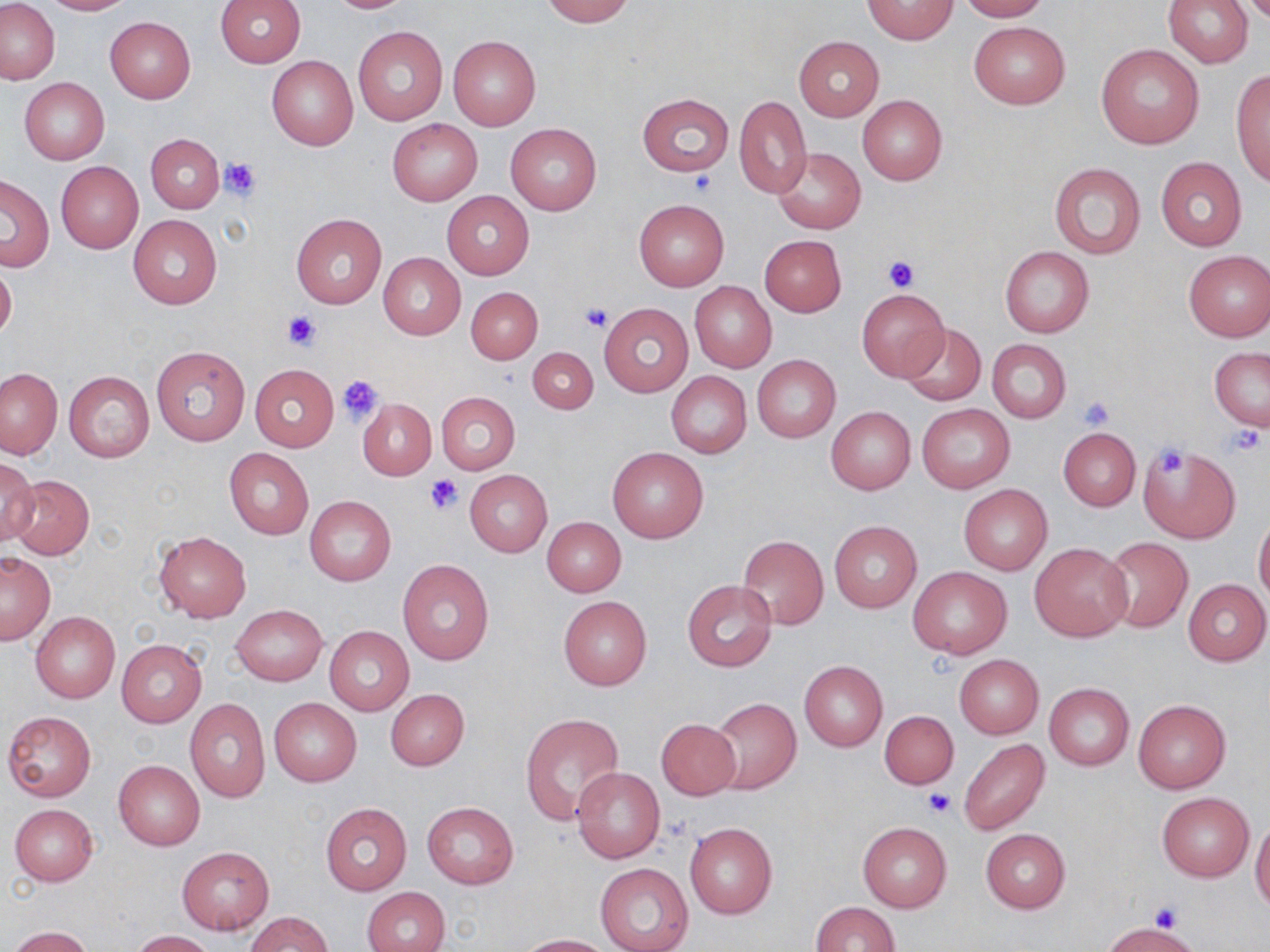

Summary:
  - Coordinate format: approximate bounding boxes as named x1/y1/x2/y2 corners in pixels
  - Platelet locations: (x1=221, y1=158, x2=261, y2=201), (x1=689, y1=172, x2=717, y2=195), (x1=880, y1=254, x2=921, y2=292), (x1=581, y1=302, x2=611, y2=332), (x1=281, y1=309, x2=323, y2=350), (x1=338, y1=372, x2=385, y2=423), (x1=1078, y1=396, x2=1117, y2=431), (x1=1223, y1=426, x2=1265, y2=461), (x1=1149, y1=443, x2=1190, y2=482), (x1=424, y1=473, x2=463, y2=515), (x1=922, y1=789, x2=954, y2=819), (x1=1150, y1=902, x2=1181, y2=934)
  - Uninfected red blood cell locations: (x1=1, y1=0, x2=60, y2=85), (x1=37, y1=0, x2=137, y2=15), (x1=324, y1=0, x2=418, y2=13), (x1=541, y1=0, x2=633, y2=26), (x1=863, y1=0, x2=957, y2=44), (x1=958, y1=0, x2=1048, y2=21), (x1=214, y1=1, x2=307, y2=66), (x1=1164, y1=1, x2=1253, y2=68), (x1=104, y1=16, x2=196, y2=103), (x1=968, y1=21, x2=1070, y2=110), (x1=353, y1=25, x2=447, y2=126), (x1=448, y1=35, x2=541, y2=131), (x1=794, y1=36, x2=885, y2=120), (x1=1096, y1=44, x2=1205, y2=150), (x1=267, y1=54, x2=359, y2=151), (x1=1231, y1=67, x2=1270, y2=187), (x1=20, y1=78, x2=109, y2=165), (x1=638, y1=93, x2=733, y2=177), (x1=857, y1=94, x2=948, y2=185), (x1=734, y1=96, x2=812, y2=197), (x1=386, y1=118, x2=482, y2=207), (x1=506, y1=123, x2=601, y2=216), (x1=146, y1=133, x2=225, y2=214), (x1=773, y1=147, x2=866, y2=234), (x1=1156, y1=157, x2=1247, y2=250), (x1=56, y1=162, x2=142, y2=254), (x1=1048, y1=163, x2=1146, y2=259), (x1=0, y1=175, x2=54, y2=271), (x1=442, y1=190, x2=534, y2=280), (x1=634, y1=200, x2=728, y2=291), (x1=290, y1=212, x2=387, y2=309), (x1=128, y1=214, x2=223, y2=310), (x1=759, y1=234, x2=846, y2=317), (x1=1000, y1=245, x2=1094, y2=337), (x1=1184, y1=250, x2=1270, y2=343), (x1=378, y1=252, x2=466, y2=339), (x1=0, y1=258, x2=17, y2=344), (x1=690, y1=281, x2=777, y2=372), (x1=467, y1=287, x2=543, y2=363), (x1=857, y1=288, x2=950, y2=380), (x1=599, y1=304, x2=693, y2=397), (x1=897, y1=322, x2=985, y2=406), (x1=987, y1=340, x2=1071, y2=422), (x1=150, y1=344, x2=250, y2=446), (x1=527, y1=347, x2=598, y2=414), (x1=1210, y1=347, x2=1269, y2=430), (x1=751, y1=355, x2=841, y2=443), (x1=249, y1=363, x2=339, y2=451), (x1=1, y1=368, x2=62, y2=459), (x1=64, y1=371, x2=154, y2=462), (x1=666, y1=372, x2=751, y2=457), (x1=435, y1=392, x2=520, y2=475), (x1=358, y1=399, x2=437, y2=480), (x1=917, y1=403, x2=1015, y2=493), (x1=825, y1=406, x2=915, y2=494), (x1=1058, y1=428, x2=1141, y2=511), (x1=1139, y1=444, x2=1242, y2=544), (x1=608, y1=446, x2=709, y2=543), (x1=225, y1=447, x2=314, y2=539), (x1=0, y1=456, x2=40, y2=546), (x1=465, y1=469, x2=552, y2=557), (x1=9, y1=476, x2=95, y2=559), (x1=958, y1=484, x2=1052, y2=574), (x1=304, y1=496, x2=396, y2=585), (x1=1253, y1=513, x2=1270, y2=606), (x1=542, y1=517, x2=626, y2=597), (x1=829, y1=521, x2=922, y2=613), (x1=153, y1=531, x2=250, y2=621), (x1=737, y1=535, x2=828, y2=629), (x1=1102, y1=537, x2=1193, y2=633), (x1=1029, y1=542, x2=1132, y2=641), (x1=0, y1=552, x2=55, y2=644), (x1=398, y1=559, x2=494, y2=665), (x1=907, y1=564, x2=1012, y2=660), (x1=1183, y1=578, x2=1270, y2=666), (x1=682, y1=580, x2=778, y2=673), (x1=558, y1=595, x2=652, y2=691), (x1=231, y1=605, x2=327, y2=685), (x1=30, y1=611, x2=120, y2=703), (x1=323, y1=626, x2=413, y2=716), (x1=116, y1=639, x2=206, y2=727), (x1=954, y1=655, x2=1044, y2=738), (x1=799, y1=660, x2=888, y2=752), (x1=1044, y1=683, x2=1134, y2=770), (x1=385, y1=689, x2=469, y2=770), (x1=708, y1=697, x2=801, y2=794), (x1=269, y1=698, x2=361, y2=786), (x1=185, y1=699, x2=271, y2=802), (x1=1131, y1=700, x2=1230, y2=794), (x1=880, y1=710, x2=959, y2=790), (x1=2, y1=711, x2=97, y2=802), (x1=519, y1=713, x2=625, y2=828), (x1=656, y1=718, x2=741, y2=800), (x1=958, y1=739, x2=1049, y2=837), (x1=113, y1=759, x2=205, y2=850), (x1=572, y1=766, x2=665, y2=863), (x1=1157, y1=792, x2=1254, y2=881), (x1=422, y1=802, x2=518, y2=889), (x1=319, y1=803, x2=413, y2=896), (x1=8, y1=804, x2=98, y2=886), (x1=1250, y1=818, x2=1270, y2=914), (x1=857, y1=821, x2=952, y2=913), (x1=684, y1=822, x2=777, y2=919), (x1=980, y1=828, x2=1071, y2=913), (x1=177, y1=847, x2=274, y2=935), (x1=596, y1=864, x2=693, y2=952), (x1=361, y1=886, x2=450, y2=952), (x1=809, y1=902, x2=900, y2=952), (x1=246, y1=912, x2=332, y2=951), (x1=1103, y1=922, x2=1201, y2=952), (x1=9, y1=926, x2=93, y2=952), (x1=129, y1=930, x2=215, y2=951), (x1=515, y1=933, x2=613, y2=951)
  - Slide-level diagnosis: negative for blood parasites
  - Magnification: 1000x
  - Preparation: thin blood smear
  - Modality: light microscopy
  - Stain: May-Grünwald-Giemsa
  - Field of view: single
  - Image size: 1270×952 pixels